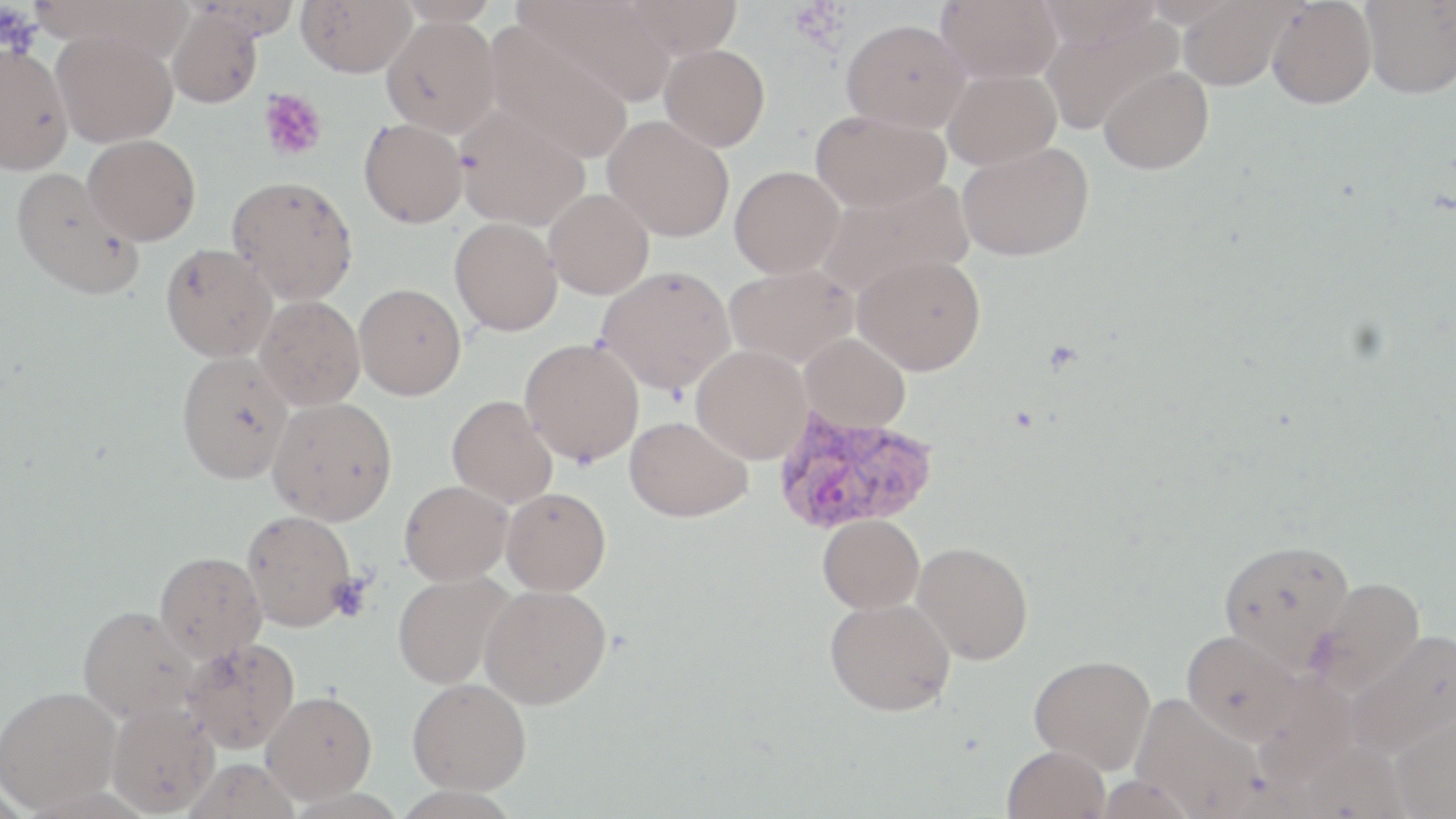
Summary:
  - Coordinate format: approximate bounding boxes as (x1,y1)-(x2,y2) corner pairs in pixels
  - Uninfected red blood cell locations: (297,0)-(416,77), (392,0)-(504,25), (515,0)-(677,106), (617,0)-(743,59), (936,0)-(1062,84), (1178,0)-(1291,90), (1034,1)-(1164,50), (1267,1)-(1376,109), (1360,2)-(1456,99), (167,7)-(264,107), (1038,10)-(1182,135), (382,15)-(500,137), (841,18)-(969,133), (484,26)-(634,163), (51,28)-(178,148), (0,44)-(72,175), (660,44)-(770,151), (1099,66)-(1213,174), (942,68)-(1061,169), (455,107)-(591,231), (810,110)-(950,213), (602,115)-(734,242), (358,118)-(468,228), (83,135)-(200,245), (957,141)-(1094,261), (730,165)-(844,278), (10,167)-(144,300), (227,175)-(358,305), (816,179)-(974,298), (544,189)-(654,299), (450,217)-(563,336), (160,243)-(278,362), (853,252)-(986,375), (724,264)-(858,368), (595,265)-(735,395), (353,283)-(466,400), (255,295)-(364,411), (799,333)-(911,431), (520,337)-(644,466), (691,345)-(812,463), (175,351)-(292,484), (446,395)-(558,509), (267,396)-(397,525), (624,416)-(752,522), (399,480)-(512,585), (501,487)-(611,595), (241,510)-(357,632), (817,514)-(924,613), (1217,539)-(1355,669), (911,542)-(1033,665), (154,551)-(266,662), (392,571)-(514,689), (1306,577)-(1425,695), (479,584)-(611,709), (825,598)-(955,716), (78,606)-(200,723), (1181,629)-(1304,744), (1345,631)-(1456,756), (181,637)-(300,754), (1029,654)-(1156,773), (407,678)-(531,794), (0,686)-(122,811), (261,690)-(377,804), (1130,694)-(1267,817), (106,701)-(218,817), (1388,709)-(1456,819), (1002,744)-(1111,819)
  - Plasmodium vivax-infected red blood cell locations: (771,407)-(939,535)
  - Platelet locations: (0,6)-(43,58), (257,88)-(327,162), (328,576)-(372,621)
  - Slide-level diagnosis: Plasmodium vivax
  - Stain: May-Grünwald-Giemsa
  - Modality: optical microscopy
  - Magnification: 1000x
  - Preparation: thin blood smear
  - Field of view: one of a larger specimen
  - Image size: 1456×819 pixels